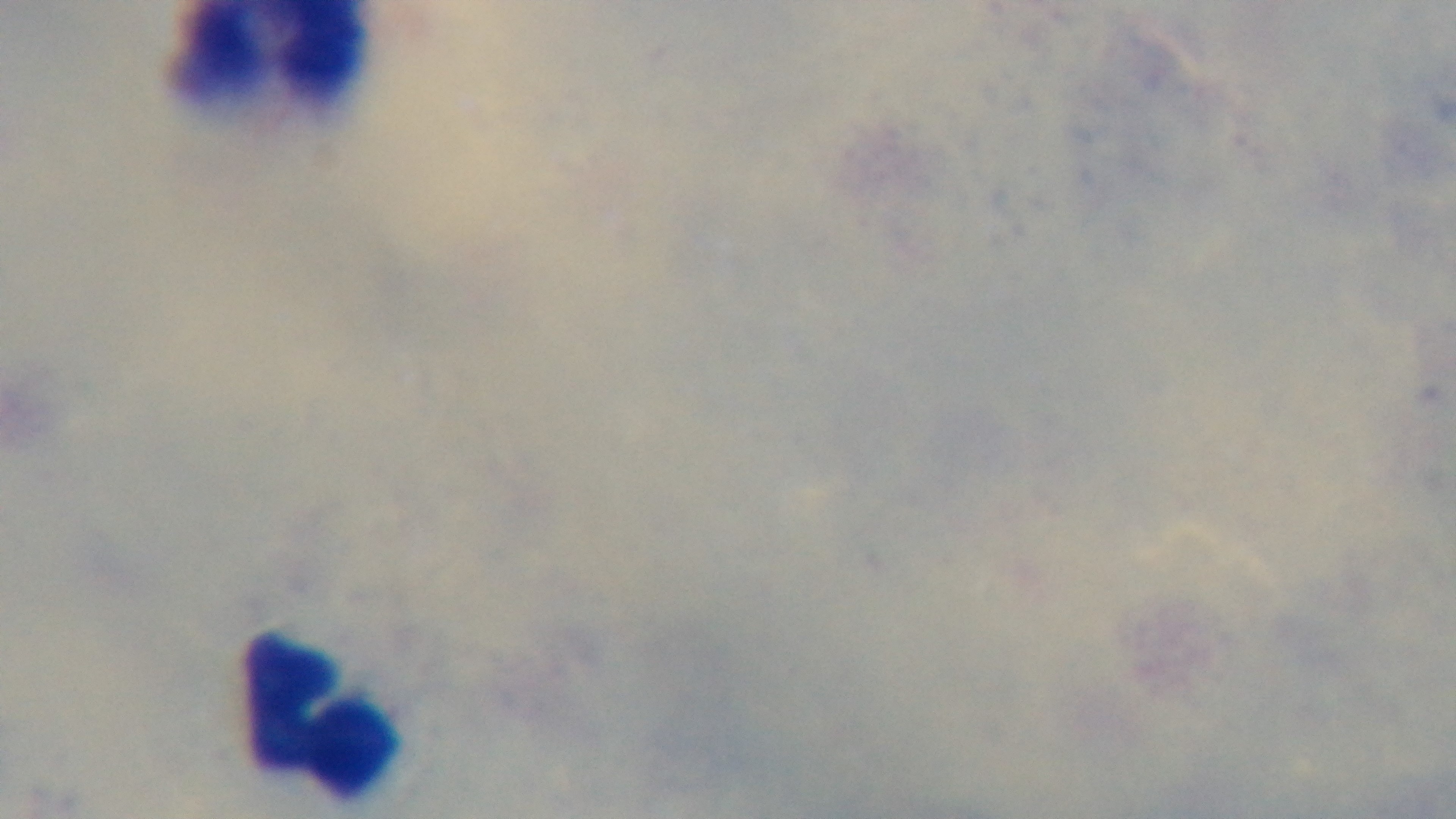

Summary:
  - Stain: Giemsa
  - Capture: mounted 4K digital camera
  - Objective: 100x oil immersion
  - Field of view: one from the slide
  - Modality: light microscopy
  - Preparation: thick blood film
  - Malaria status: uninfected